Point out each Plasmodium parasite.
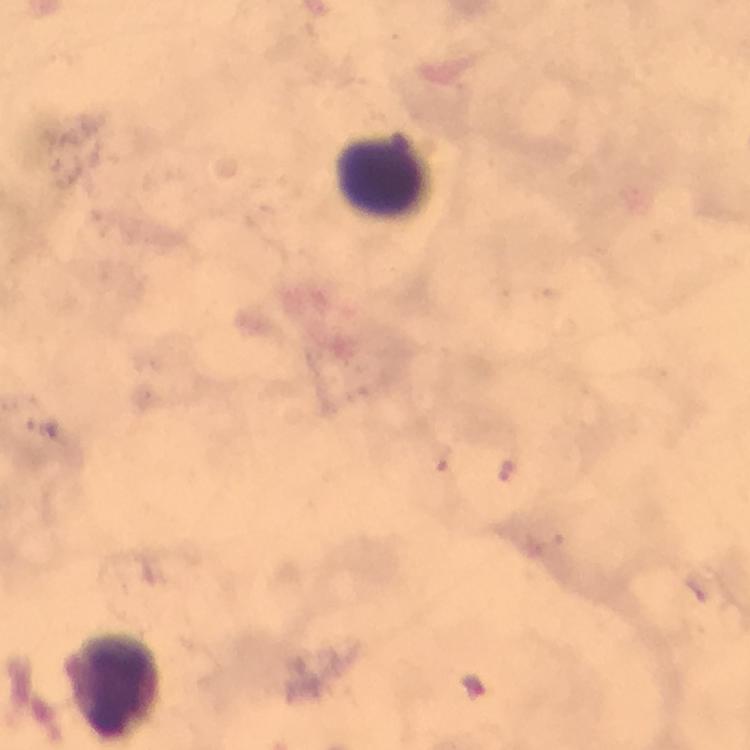
Approximate centers as [x, y] in pixels.
Plasmodium parasites: [506, 474].

Leukocyte locations: [381, 175], [111, 684]. Image is 750×750 pixels. Smartphone photograph taken through a microscope. At 100x magnification. Giemsa-stained preparation. Immersion oil was used. Cropped region of a single field of view. From a diagnostic examination for malaria. Thick smear.